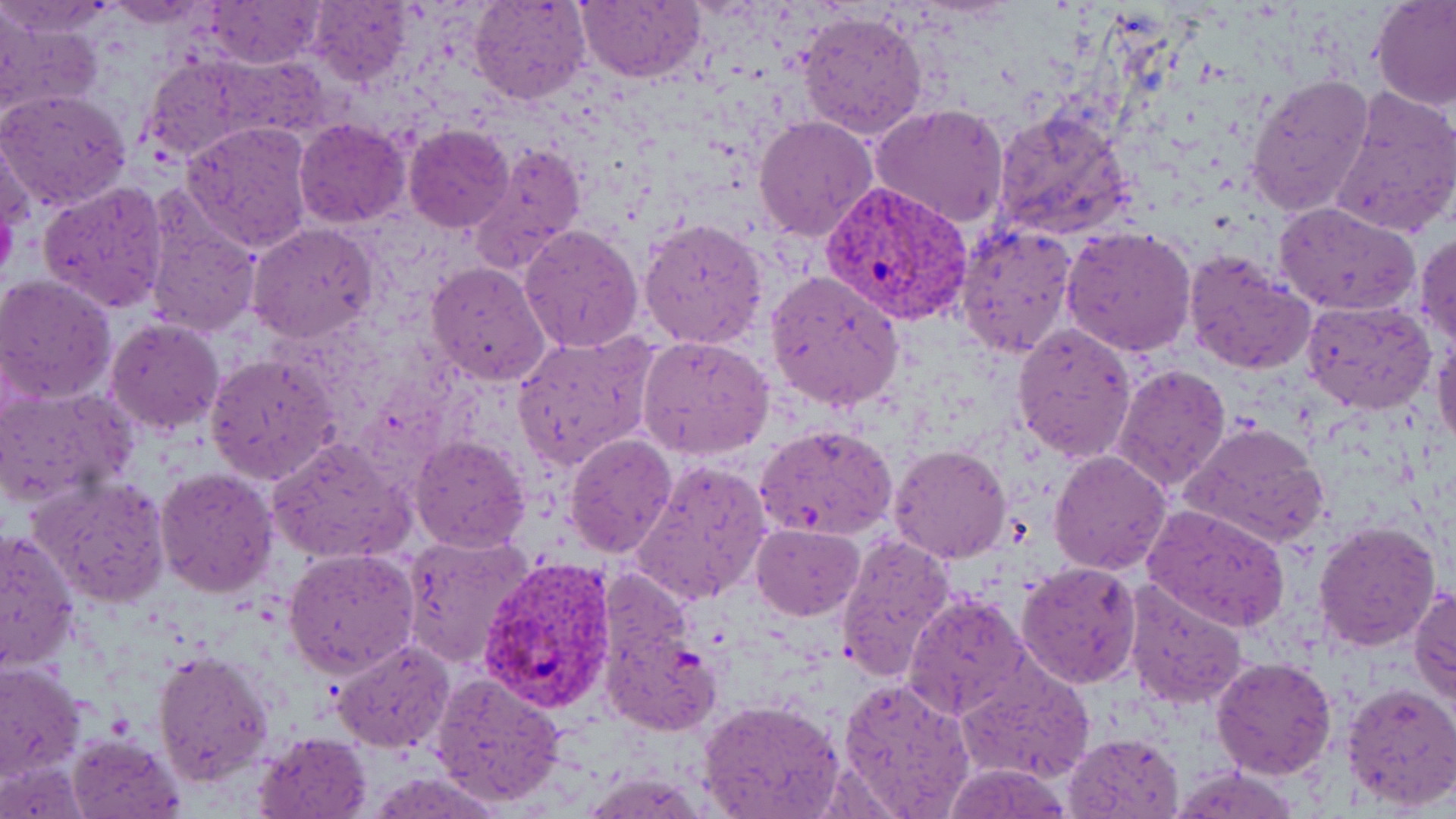 Approximate bounding boxes as named x1/y1/x2/y2 corners in pixels. Plasmodium vivax-infected red blood cell locations: (x1=822, y1=180, x2=973, y2=326), (x1=479, y1=555, x2=617, y2=714). Uninfected red blood cell locations: (x1=103, y1=0, x2=216, y2=25), (x1=307, y1=0, x2=414, y2=87), (x1=470, y1=0, x2=592, y2=106), (x1=1371, y1=0, x2=1456, y2=111), (x1=0, y1=1, x2=114, y2=35), (x1=205, y1=1, x2=324, y2=68), (x1=575, y1=1, x2=704, y2=83), (x1=798, y1=10, x2=928, y2=140), (x1=140, y1=58, x2=255, y2=162), (x1=1246, y1=73, x2=1374, y2=219), (x1=0, y1=87, x2=132, y2=211), (x1=1328, y1=88, x2=1456, y2=240), (x1=869, y1=102, x2=1011, y2=230), (x1=991, y1=107, x2=1136, y2=242), (x1=753, y1=117, x2=877, y2=243), (x1=293, y1=118, x2=410, y2=228), (x1=182, y1=121, x2=313, y2=252), (x1=404, y1=125, x2=515, y2=232), (x1=0, y1=135, x2=32, y2=252), (x1=476, y1=143, x2=584, y2=273), (x1=38, y1=179, x2=169, y2=312), (x1=142, y1=200, x2=263, y2=339), (x1=1273, y1=200, x2=1421, y2=316), (x1=640, y1=218, x2=768, y2=352), (x1=245, y1=222, x2=379, y2=343), (x1=954, y1=222, x2=1077, y2=362), (x1=518, y1=224, x2=644, y2=354), (x1=1062, y1=225, x2=1197, y2=357), (x1=1415, y1=230, x2=1456, y2=349), (x1=1183, y1=249, x2=1315, y2=374), (x1=426, y1=262, x2=551, y2=385), (x1=768, y1=270, x2=904, y2=411), (x1=1, y1=274, x2=117, y2=403), (x1=1302, y1=299, x2=1437, y2=414), (x1=106, y1=317, x2=224, y2=436), (x1=1013, y1=323, x2=1136, y2=460), (x1=512, y1=331, x2=659, y2=468), (x1=1432, y1=331, x2=1456, y2=450), (x1=638, y1=335, x2=774, y2=458), (x1=204, y1=353, x2=340, y2=485), (x1=1113, y1=362, x2=1232, y2=493), (x1=0, y1=386, x2=134, y2=509), (x1=1181, y1=421, x2=1330, y2=551), (x1=755, y1=423, x2=898, y2=543), (x1=565, y1=432, x2=678, y2=559), (x1=409, y1=435, x2=530, y2=553), (x1=267, y1=438, x2=413, y2=564), (x1=889, y1=443, x2=1012, y2=564), (x1=1049, y1=449, x2=1175, y2=575), (x1=633, y1=457, x2=773, y2=603), (x1=153, y1=465, x2=277, y2=597), (x1=28, y1=476, x2=170, y2=608), (x1=1143, y1=503, x2=1291, y2=631), (x1=1311, y1=518, x2=1441, y2=651), (x1=751, y1=523, x2=864, y2=620), (x1=0, y1=529, x2=80, y2=674), (x1=833, y1=531, x2=955, y2=679), (x1=400, y1=534, x2=533, y2=665), (x1=283, y1=548, x2=420, y2=677), (x1=1017, y1=561, x2=1143, y2=689), (x1=1123, y1=578, x2=1249, y2=710), (x1=1410, y1=584, x2=1455, y2=703), (x1=903, y1=593, x2=1030, y2=719), (x1=606, y1=618, x2=723, y2=739), (x1=331, y1=639, x2=454, y2=752), (x1=152, y1=648, x2=273, y2=785), (x1=1210, y1=656, x2=1338, y2=779), (x1=0, y1=661, x2=87, y2=782), (x1=957, y1=664, x2=1094, y2=782), (x1=430, y1=673, x2=566, y2=806), (x1=836, y1=675, x2=975, y2=817), (x1=1339, y1=681, x2=1456, y2=813), (x1=700, y1=698, x2=844, y2=818), (x1=253, y1=730, x2=372, y2=818), (x1=66, y1=732, x2=185, y2=817), (x1=1064, y1=733, x2=1182, y2=818), (x1=1170, y1=764, x2=1302, y2=819), (x1=584, y1=772, x2=705, y2=817). Slide-level diagnosis: Plasmodium vivax. Thin blood smear. Image is 1456×819 pixels. Captured at 1000x magnification. May-Grünwald-Giemsa stain. Single field of view. Optical microscopy.